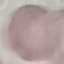
Summary:
  - Malaria status: uninfected
  - Preparation: thin blood film
  - Capture: smartphone through the microscope eyepiece
  - Image type: automatically extracted cell patch, resized to 64 × 64 pixels
  - Stain: Giemsa